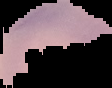

Summary:
  - Malaria status: uninfected
  - Image type: segmented cell region on a black background
  - Image size: 112×88 pixels
  - Preparation: thin blood film